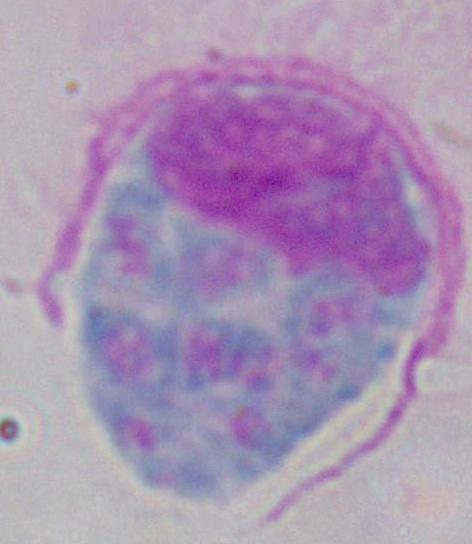
modality = photomicrograph
identification = leukocyte
magnification = 1000x